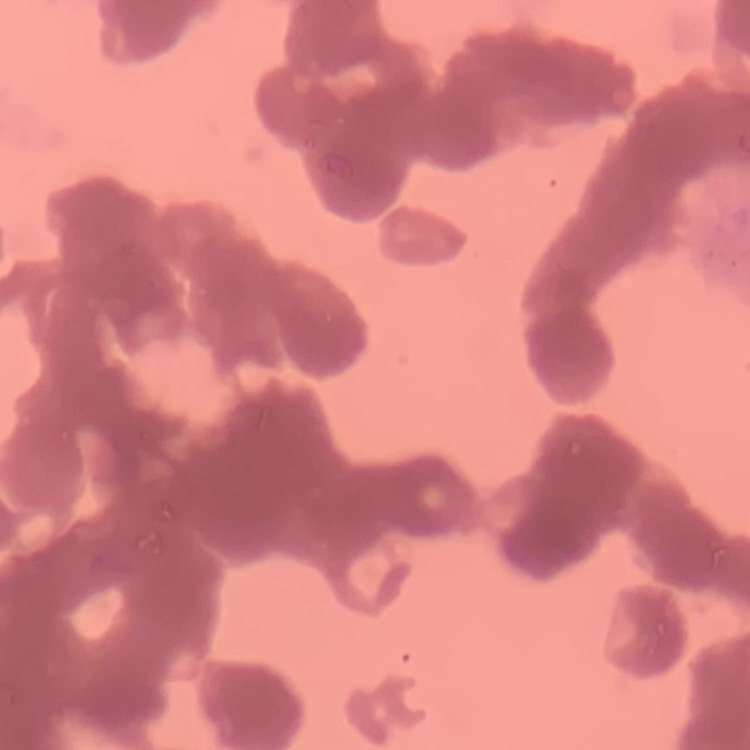

Summary:
  - Erythrocyte morphology: rouleaux formation
  - Stain: Field's or Giemsa
  - Image type: square crop of a larger photomicrograph
  - Preparation: thin blood smear